Evaluate for Plasmodium parasites.
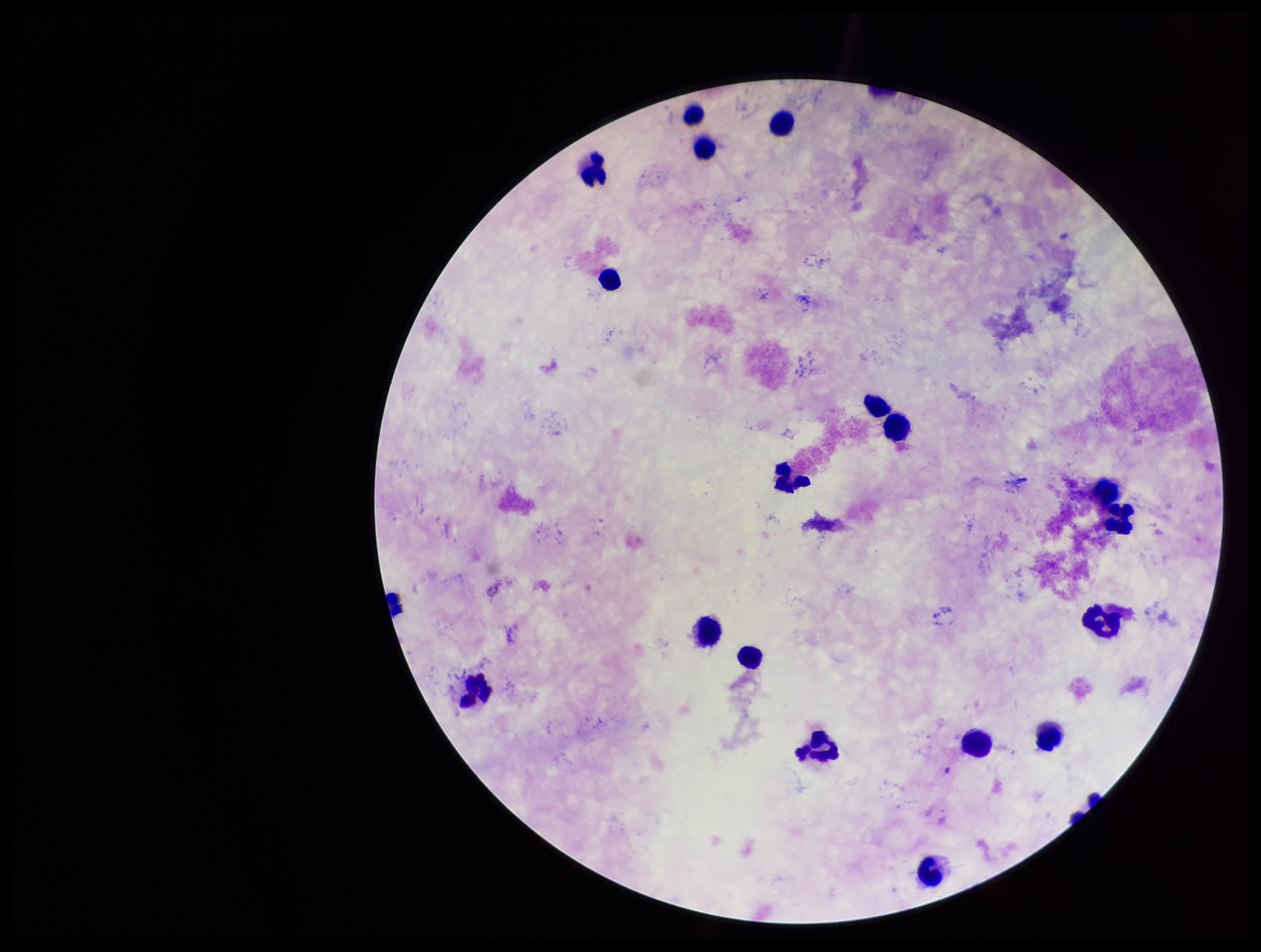

None detected.

One field from this slide. Patient malaria status: negative. Image is 1261×952 pixels. Preparation: thick. Smartphone photograph taken through the eyepiece of a microscope. Stained with Giemsa. Leukocyte count: 20. Parasite count: 0.